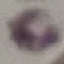
result = no malaria parasites detected
capture = smartphone through the microscope eyepiece
stain = Giemsa
preparation = thin blood smear
image type = automatically extracted cell patch, resized to 64 × 64 pixels